State which parasite is depicted.
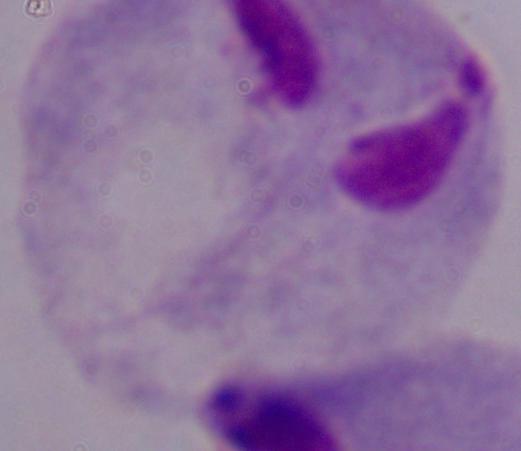

This is a trichomonad.

magnification = 1000x
modality = photomicrograph